Comment on the morphology of the red blood cells.
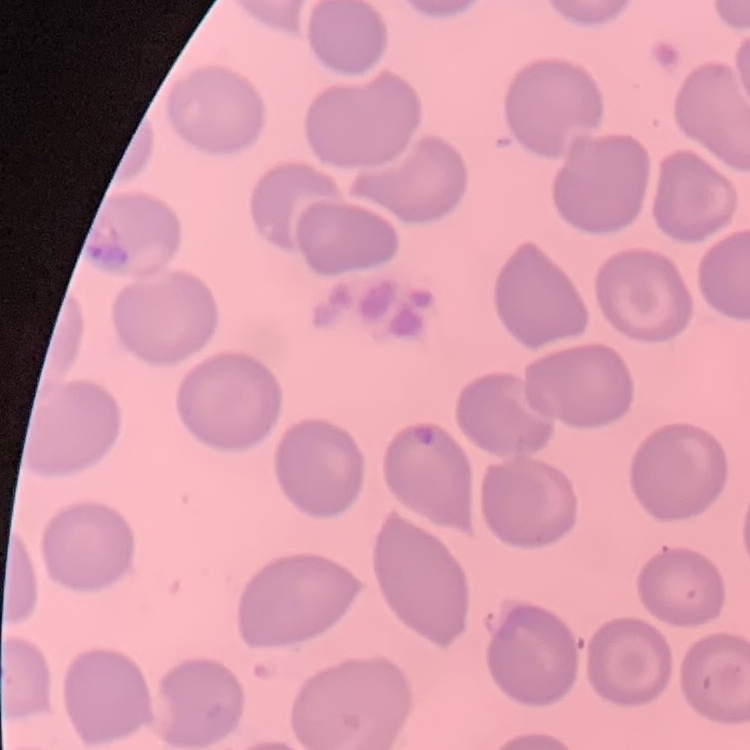

No rouleaux formation.

Thin blood film. Field's or Giemsa stain. Square crop of a larger photomicrograph.